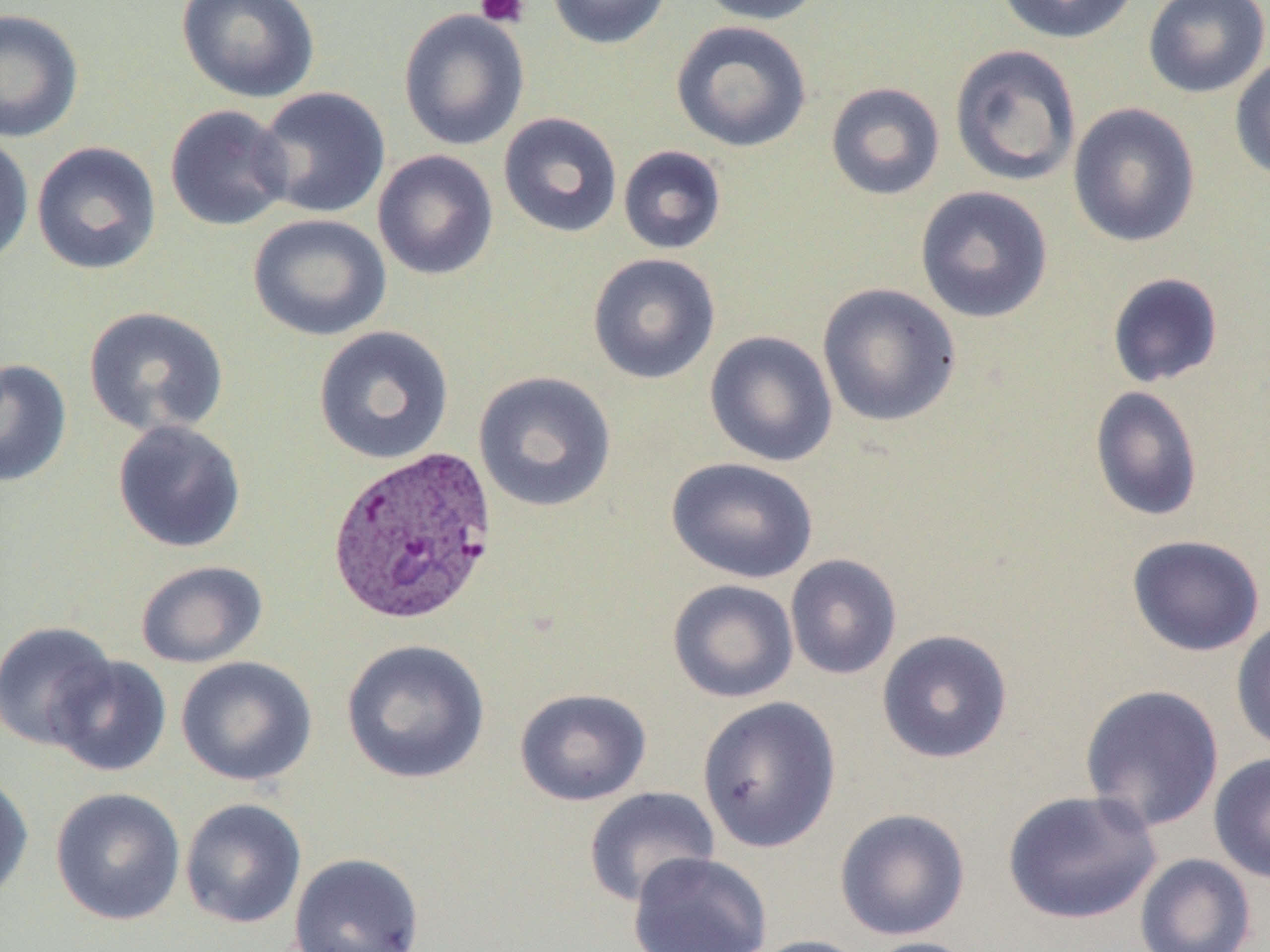 Approximate bounding boxes as [x1, y1, x2, y2] in pixels. Plasmodium vivax-infected red blood cell locations: [326, 444, 500, 626]. Uninfected red blood cell locations: [175, 0, 321, 104], [546, 0, 673, 50], [694, 0, 828, 25], [995, 0, 1139, 45], [1142, 0, 1270, 99], [0, 8, 84, 144], [398, 9, 531, 152], [670, 20, 813, 153], [949, 44, 1082, 188], [1229, 55, 1270, 184], [825, 81, 945, 201], [253, 86, 391, 219], [1067, 102, 1201, 249], [164, 104, 295, 232], [498, 112, 623, 239], [0, 132, 34, 268], [31, 141, 163, 276], [618, 145, 727, 254], [372, 149, 498, 281], [914, 185, 1054, 323], [248, 213, 393, 342], [587, 253, 721, 385], [1107, 272, 1224, 388], [817, 283, 962, 428], [83, 305, 229, 438], [313, 325, 454, 465], [704, 330, 838, 468], [0, 358, 72, 488], [473, 370, 618, 513], [1089, 386, 1203, 522], [111, 419, 246, 554], [665, 456, 819, 584], [1126, 534, 1266, 657], [784, 553, 902, 680], [134, 559, 269, 668], [667, 578, 799, 703], [1231, 616, 1270, 755], [0, 620, 118, 751], [876, 628, 1014, 764], [340, 638, 492, 785], [48, 655, 172, 777], [175, 655, 318, 787], [1079, 684, 1225, 832], [514, 688, 653, 806], [696, 696, 842, 852], [1208, 752, 1270, 883], [0, 770, 33, 905], [583, 786, 721, 908], [50, 787, 186, 925], [1002, 789, 1162, 925], [180, 797, 307, 929], [834, 807, 971, 941], [289, 851, 425, 952], [627, 851, 772, 952], [1134, 853, 1258, 952], [746, 935, 875, 952], [859, 936, 985, 952]. Platelet locations: [475, 0, 530, 28]. Slide-level diagnosis: Plasmodium vivax. Captured at 1000x magnification. Single field of view. Thin blood smear. Optical microscopy. Image is 1270×952 pixels.